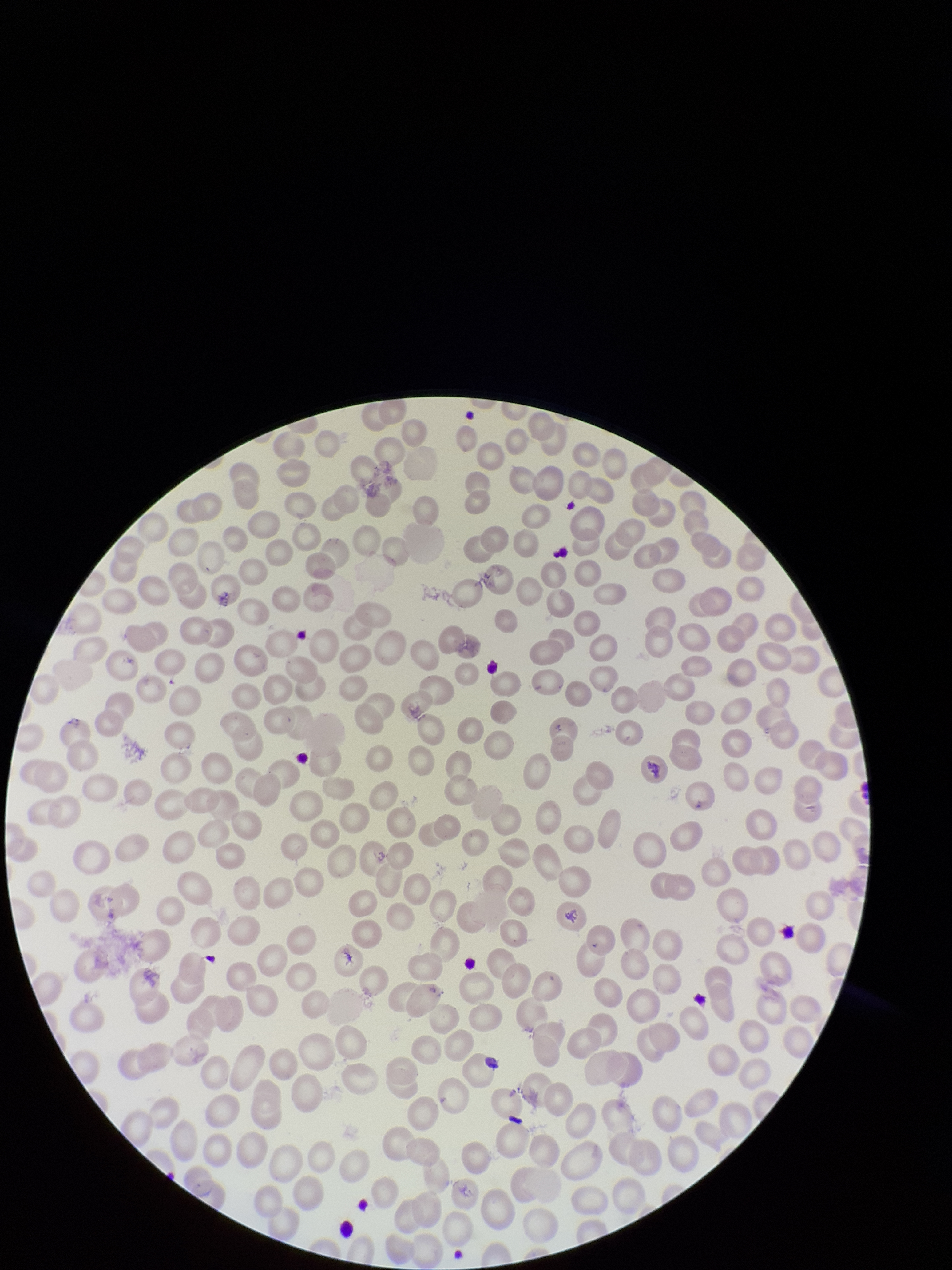
parasitized red blood cells = none identified
capture = smartphone photograph through the microscope eyepiece
preparation = thin blood smear
patient malaria status = negative
parasitized red blood cell count = 0
field of view = one from this slide
image size = 952×1270 pixels
red blood cell count = 263
stain = Giemsa